Assess this cell for malaria.
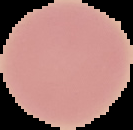

Uninfected.

{
  "preparation": "thin blood film",
  "image_type": "segmented cell region with the area outside set to black",
  "image_size": "133×130 pixels"
}